Comment on the morphology of the red blood cells.
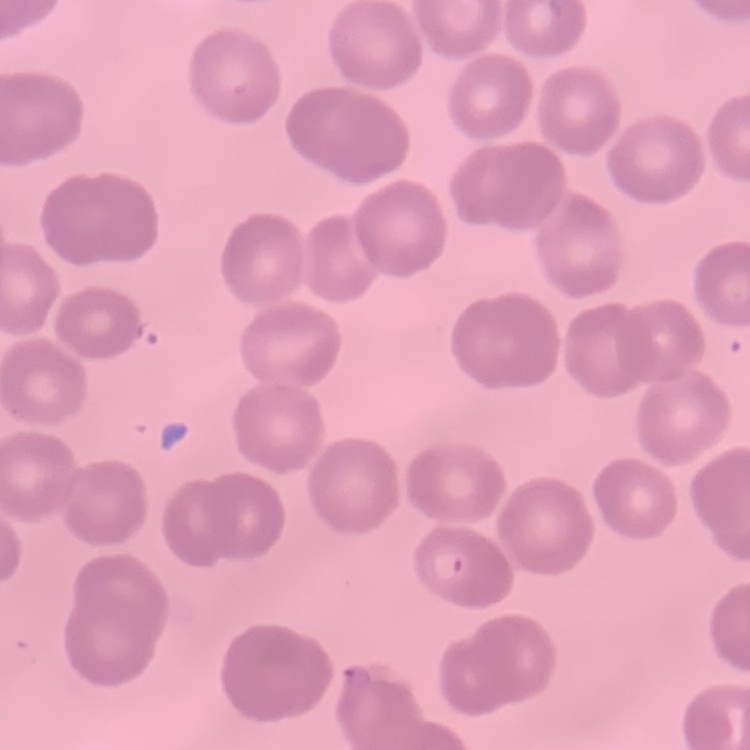
No rouleaux formation.

Stained with either Field's or Giemsa. Square crop of a larger photomicrograph. Thin peripheral smear.